Classify this cell by malaria status.
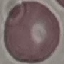
Uninfected.

Thin blood film. Acquired by smartphone through the microscope eyepiece. Automatically extracted cell patch, resized to 64 × 64 pixels. Giemsa stain.